Point out leukocytes.
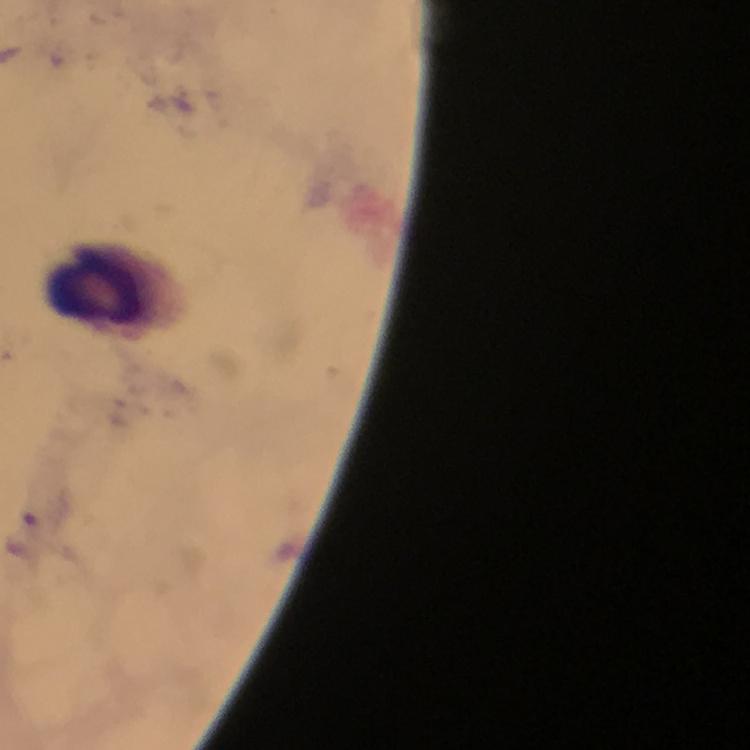

Approximate centers as (x, y) in pixels.
Leukocytes: (99, 289).

malaria parasites = none detected
magnification = 100x
image size = 750×750 pixels
stain = Giemsa
cropped from = a single field of view
context = from a malaria diagnostic workup
preparation = thick blood smear
capture = smartphone photograph through a microscope
immersion oil = applied